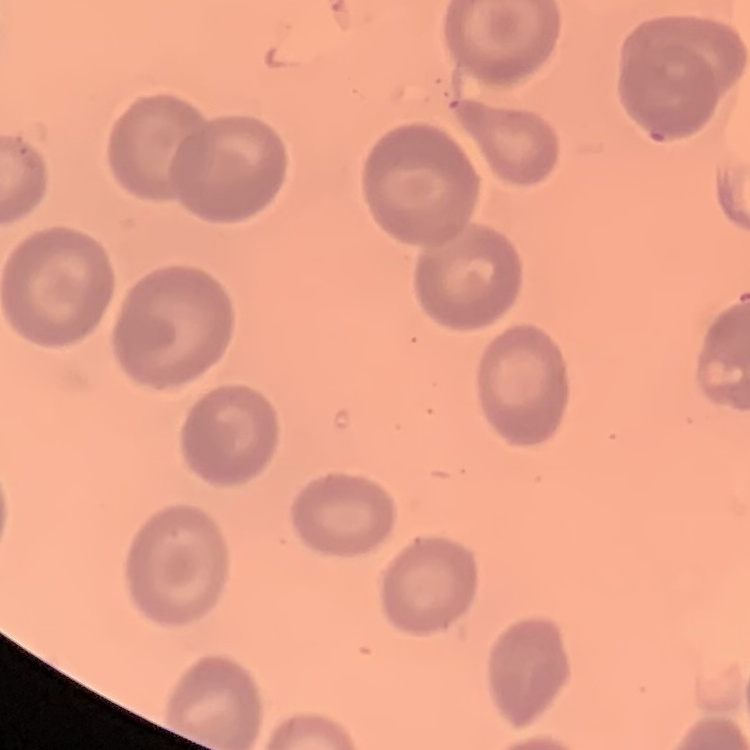
The red blood cells show no rouleaux formation. One tile cut from a larger photomicrograph. Thin peripheral smear. Field's or Giemsa stain.